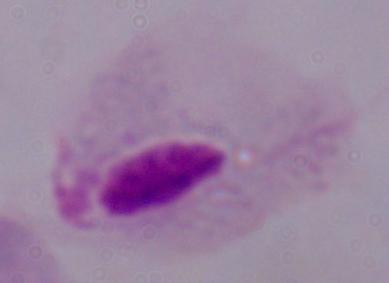

{
  "identification": "trichomonad",
  "modality": "micrograph",
  "magnification": "1000x"
}